Describe the morphology of the red blood cells.
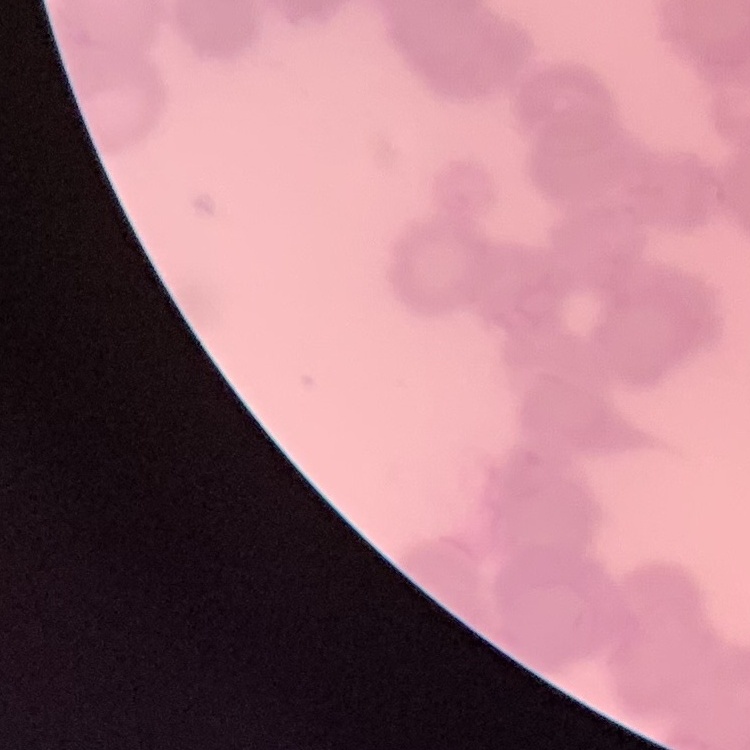
They show rouleaux formation.

image type = one tile cut from a larger photomicrograph
preparation = thin blood film
stain = Field's or Giemsa